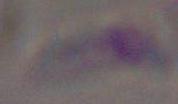
Summary:
  - Magnification: 1000x
  - Identification: Toxoplasma gondii
  - Modality: photomicrograph